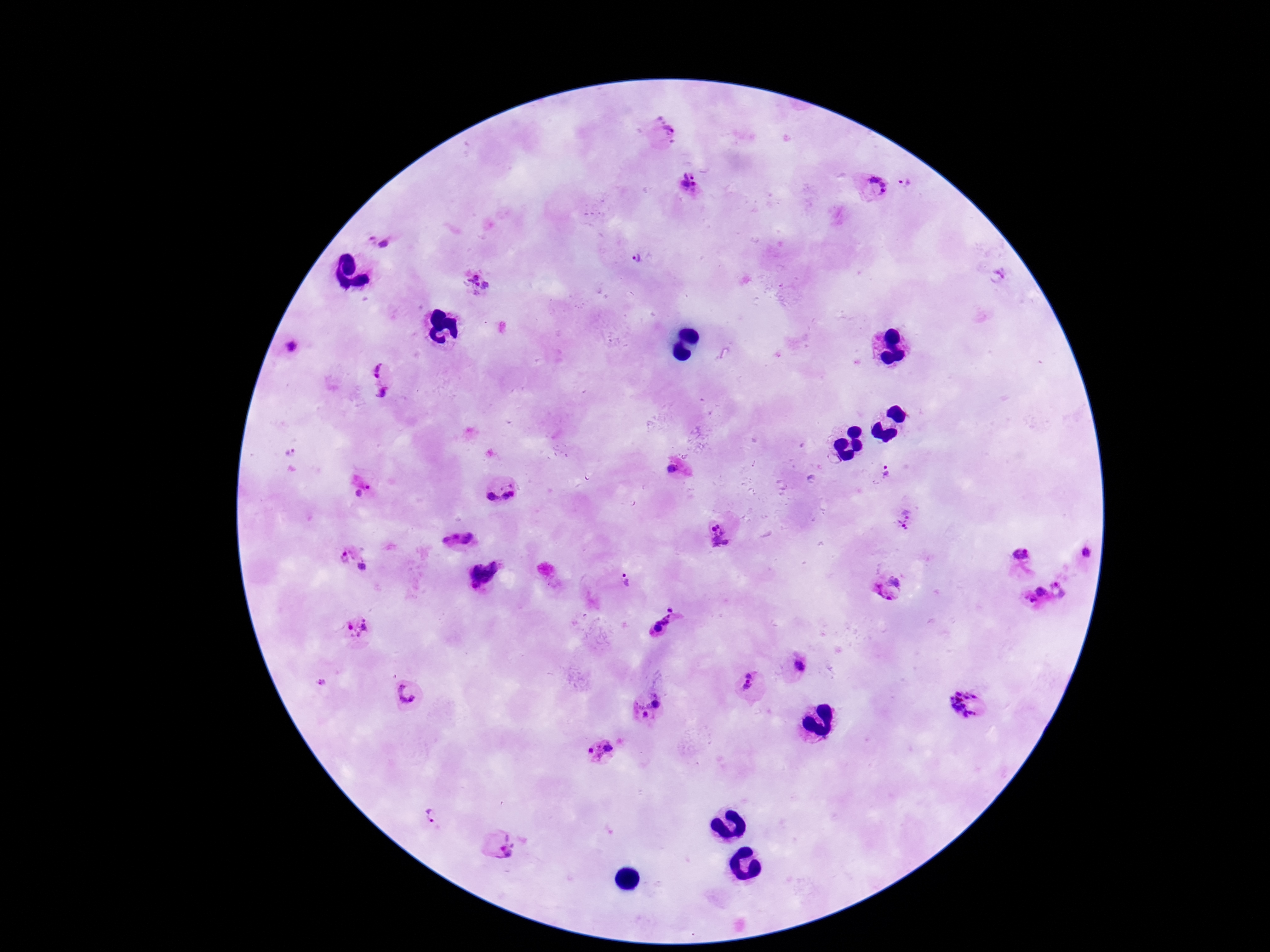
Approximate centers as {x, y} in pixels. Plasmodium parasite locations: {663, 134}, {904, 183}, {689, 186}, {874, 186}, {381, 242}, {638, 259}, {999, 276}, {475, 282}, {291, 348}, {380, 367}, {382, 394}, {291, 451}, {674, 469}, {887, 471}, {365, 491}, {500, 492}, {905, 518}, {718, 526}, {713, 528}, {456, 536}, {720, 541}, {345, 554}, {1087, 554}, {1021, 555}, {362, 566}, {483, 571}, {896, 577}, {626, 582}, {1058, 588}, {1040, 592}, {884, 595}, {1030, 601}, {670, 610}, {663, 620}, {358, 627}, {658, 629}, {798, 666}, {323, 682}, {746, 682}, {408, 693}, {657, 704}, {966, 706}, {640, 709}, {608, 748}, {593, 753}, {432, 815}, {499, 846}. Thick blood smear. Patient malaria status: positive. Giemsa stain. Photographed through the microscope eyepiece with a smartphone camera. Single field of view. Image is 1270×952 pixels. 100x magnification.